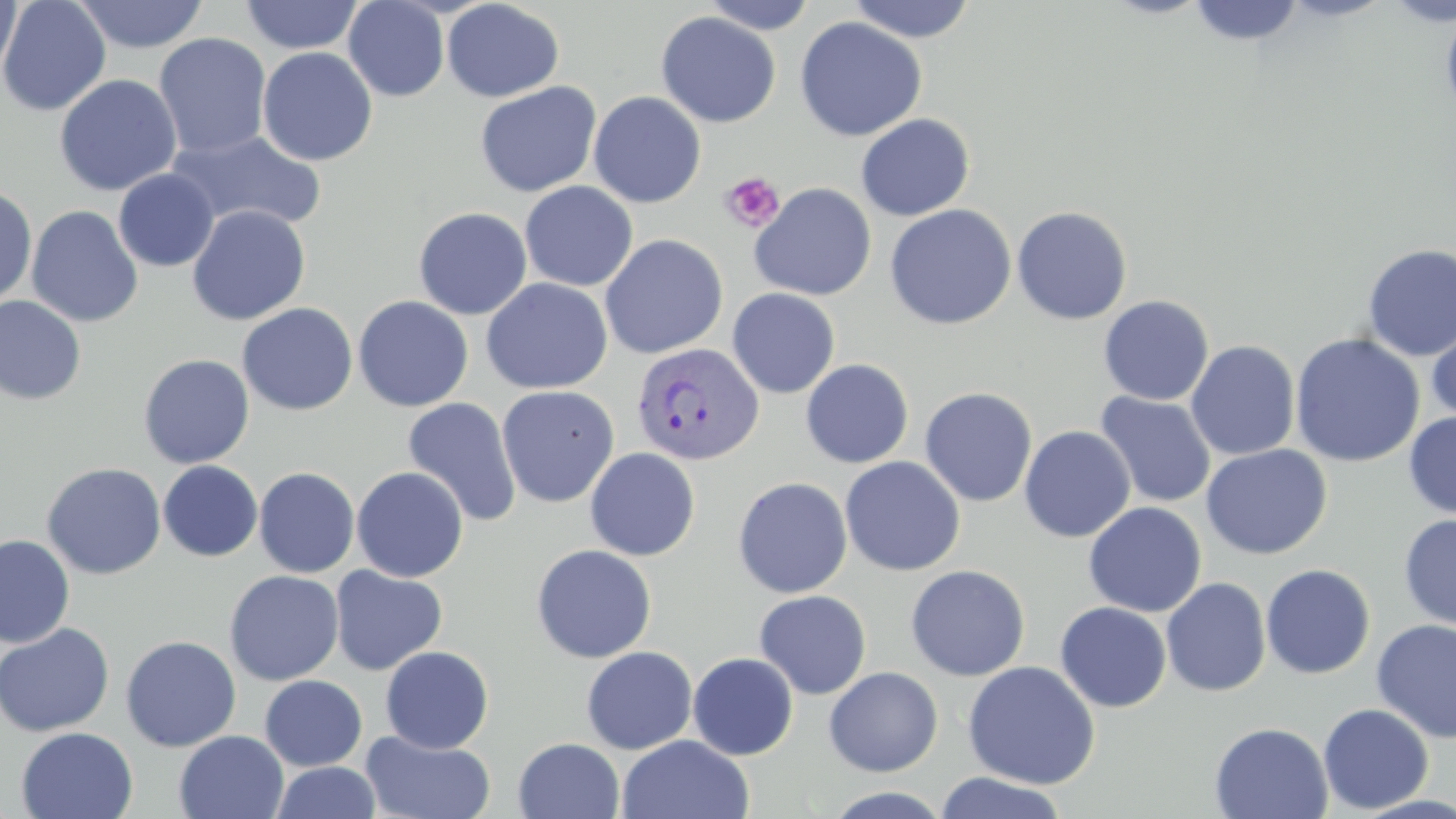
slide-level diagnosis = Plasmodium vivax
magnification = 1000x
uninfected red blood cell locations = approximate bounding boxes as [x1, y1, x2, y2] in pixels: [0, 0, 111, 116], [0, 0, 22, 87], [72, 0, 209, 53], [239, 0, 365, 55], [343, 0, 450, 102], [441, 0, 564, 102], [700, 0, 818, 35], [846, 0, 978, 43], [1280, 0, 1394, 22], [1384, 0, 1455, 27], [1187, 1, 1306, 47], [1440, 7, 1456, 125], [655, 11, 781, 128], [794, 16, 927, 142], [153, 33, 272, 159], [257, 46, 378, 166], [54, 74, 182, 197], [474, 81, 602, 198], [588, 91, 707, 208], [855, 113, 974, 222], [165, 129, 326, 233], [114, 169, 219, 272], [519, 181, 638, 291], [749, 182, 877, 300], [0, 186, 37, 307], [884, 204, 1017, 330], [26, 205, 143, 328], [187, 205, 311, 325], [1012, 206, 1133, 325], [413, 207, 533, 320], [599, 234, 728, 359], [1361, 244, 1456, 361], [481, 278, 613, 394], [727, 288, 840, 398], [0, 295, 87, 406], [353, 295, 474, 412], [1098, 295, 1214, 406], [237, 302, 358, 415], [1426, 316, 1456, 427], [1289, 333, 1425, 467], [1186, 340, 1300, 461], [138, 353, 255, 469], [800, 358, 914, 469], [496, 385, 619, 508], [919, 387, 1038, 507], [1094, 391, 1216, 508], [402, 397, 522, 527], [1403, 411, 1456, 519], [1019, 425, 1136, 543], [1201, 444, 1332, 559], [585, 448, 700, 561], [840, 456, 966, 576], [158, 461, 263, 561], [41, 462, 166, 579], [351, 466, 469, 582], [254, 467, 360, 578], [733, 477, 852, 598], [1083, 501, 1206, 617], [1398, 514, 1456, 631], [0, 533, 75, 648], [531, 544, 657, 663], [905, 564, 1030, 681], [1260, 564, 1375, 679], [329, 566, 447, 674], [224, 570, 344, 686], [1161, 578, 1271, 697], [754, 589, 872, 699], [1055, 602, 1172, 712], [1371, 619, 1456, 743], [0, 623, 115, 737], [120, 635, 241, 752], [380, 645, 494, 753], [581, 645, 698, 754], [688, 652, 799, 760], [963, 660, 1101, 790], [824, 666, 943, 776], [259, 675, 367, 771], [1317, 703, 1434, 813], [1209, 722, 1333, 819], [17, 727, 138, 819], [360, 730, 496, 818], [174, 731, 289, 818], [617, 734, 755, 819], [513, 737, 625, 819], [270, 762, 382, 819], [934, 772, 1070, 819], [820, 787, 955, 819]
stain = May-Grünwald-Giemsa
field of view = single
Plasmodium vivax-infected red blood cell locations = approximate bounding boxes as [x1, y1, x2, y2] in pixels: [631, 342, 764, 465]
preparation = thin blood smear
image size = 1456×819 pixels
modality = light microscopy
platelet locations = approximate bounding boxes as [x1, y1, x2, y2] in pixels: [719, 172, 785, 233]